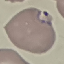 Malaria status: parasitized. Cell patch, automatically extracted from a larger field of view and resized to 64 × 64 pixels. Giemsa stain. Acquired by smartphone through the microscope eyepiece. Thin blood smear.